Outline each Plasmodium ovale-infected red blood cell.
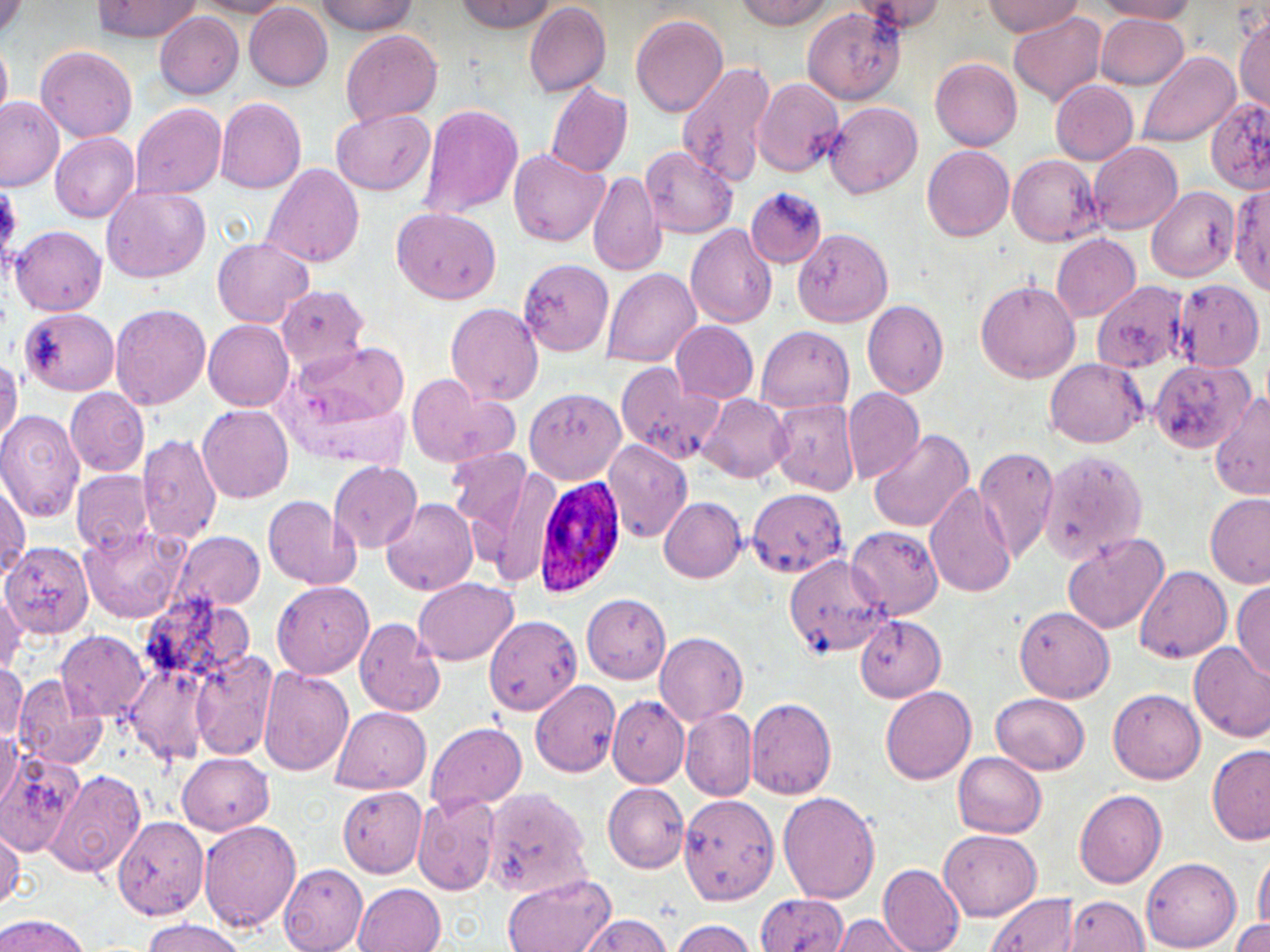

Approximate bounding boxes as (x1, y1, x2, y2) in pixels.
Plasmodium ovale-infected red blood cells: (529, 472, 631, 598).

slide-level diagnosis = Plasmodium ovale
preparation = thin blood film
image size = 1270×952 pixels
uninfected red blood cell locations = approximate bounding boxes as (x1, y1, x2, y2) in pixels: (1, 0, 25, 41), (98, 0, 197, 41), (192, 0, 295, 16), (310, 0, 417, 35), (455, 0, 557, 33), (731, 0, 837, 29), (852, 0, 945, 34), (1096, 0, 1201, 21), (979, 1, 1085, 36), (244, 2, 334, 89), (523, 2, 611, 97), (803, 6, 906, 104), (153, 10, 246, 98), (1008, 10, 1106, 106), (1094, 13, 1190, 90), (631, 14, 728, 116), (1235, 16, 1269, 111), (340, 28, 443, 128), (0, 42, 12, 119), (36, 43, 138, 141), (1138, 51, 1239, 146), (930, 57, 1022, 150), (674, 60, 778, 183), (750, 78, 845, 180), (1049, 79, 1138, 165), (545, 80, 633, 178), (214, 96, 306, 195), (1205, 96, 1270, 193), (1, 97, 64, 190), (823, 100, 924, 199), (130, 102, 226, 200), (417, 103, 524, 221), (332, 107, 435, 196), (50, 133, 139, 223), (1087, 141, 1183, 235), (922, 145, 1015, 241), (640, 146, 738, 237), (508, 148, 611, 246), (1008, 153, 1104, 246), (259, 162, 364, 268), (588, 171, 664, 279), (1227, 182, 1270, 295), (101, 183, 210, 283), (1146, 185, 1240, 281), (744, 187, 825, 267), (391, 207, 501, 305), (685, 223, 779, 328), (10, 225, 106, 316), (792, 226, 895, 326), (1051, 234, 1140, 320), (210, 236, 315, 327), (518, 257, 616, 357), (602, 268, 701, 368), (1173, 278, 1264, 370), (974, 279, 1080, 382), (1090, 279, 1191, 373), (276, 286, 369, 371), (862, 301, 949, 398), (109, 303, 211, 411), (446, 303, 544, 405), (21, 308, 119, 396), (203, 320, 294, 410), (670, 321, 759, 404), (755, 325, 855, 416), (283, 340, 410, 442), (1044, 357, 1146, 447), (1148, 357, 1253, 455), (0, 359, 19, 449), (614, 367, 721, 466), (405, 374, 521, 471), (527, 386, 627, 484), (65, 387, 148, 477), (842, 388, 924, 483), (1210, 393, 1270, 500), (699, 394, 792, 482), (769, 397, 860, 496), (199, 404, 293, 502), (0, 409, 85, 523), (868, 429, 975, 533), (137, 433, 221, 544), (600, 438, 693, 541), (974, 445, 1058, 564), (445, 448, 532, 530), (1040, 450, 1151, 565), (328, 461, 421, 552), (483, 463, 566, 588), (70, 471, 153, 556), (0, 476, 28, 575), (925, 481, 1017, 599), (745, 488, 849, 579), (1206, 493, 1270, 591), (263, 495, 361, 591), (658, 496, 747, 582), (380, 497, 477, 596), (79, 526, 190, 623), (842, 526, 942, 620), (171, 531, 265, 612), (1061, 531, 1168, 634), (2, 541, 93, 640), (783, 552, 891, 658), (1135, 565, 1229, 662), (413, 577, 520, 665), (1232, 579, 1270, 680), (272, 581, 374, 677), (0, 587, 27, 673), (581, 592, 671, 682), (137, 595, 258, 692), (1015, 605, 1114, 703), (855, 615, 947, 701), (484, 616, 582, 714), (354, 618, 446, 718), (58, 630, 149, 719), (655, 632, 748, 724), (1189, 641, 1270, 742), (190, 650, 279, 761), (124, 662, 215, 765), (0, 664, 27, 746), (259, 666, 353, 776), (15, 678, 103, 769), (531, 680, 620, 778), (880, 686, 976, 784), (1106, 686, 1205, 784), (992, 692, 1090, 774), (608, 696, 689, 786), (745, 697, 837, 799), (328, 707, 430, 795), (681, 708, 757, 799), (425, 722, 527, 812), (0, 728, 22, 816), (1207, 742, 1270, 848), (0, 749, 86, 858), (178, 753, 274, 834), (953, 753, 1046, 837), (43, 768, 145, 878), (602, 783, 688, 873), (339, 785, 428, 877), (480, 786, 594, 899), (1073, 787, 1166, 888), (778, 791, 882, 903), (676, 792, 779, 906), (412, 794, 502, 895), (113, 815, 210, 920), (197, 820, 300, 934), (0, 826, 23, 910), (938, 830, 1044, 922), (1253, 848, 1270, 940), (1143, 859, 1240, 950), (279, 864, 369, 951), (878, 865, 966, 952), (501, 873, 615, 952), (357, 883, 446, 952), (1243, 886, 1270, 952), (755, 892, 849, 952), (984, 893, 1080, 952), (1065, 895, 1149, 951), (833, 913, 921, 952), (578, 914, 672, 950), (0, 915, 90, 951), (140, 918, 249, 952), (668, 918, 757, 951), (1232, 918, 1270, 951)
field of view = one of a larger specimen
modality = optical microscopy
magnification = 1000x
stain = May-Grünwald-Giemsa